Describe the morphology of the red blood cells.
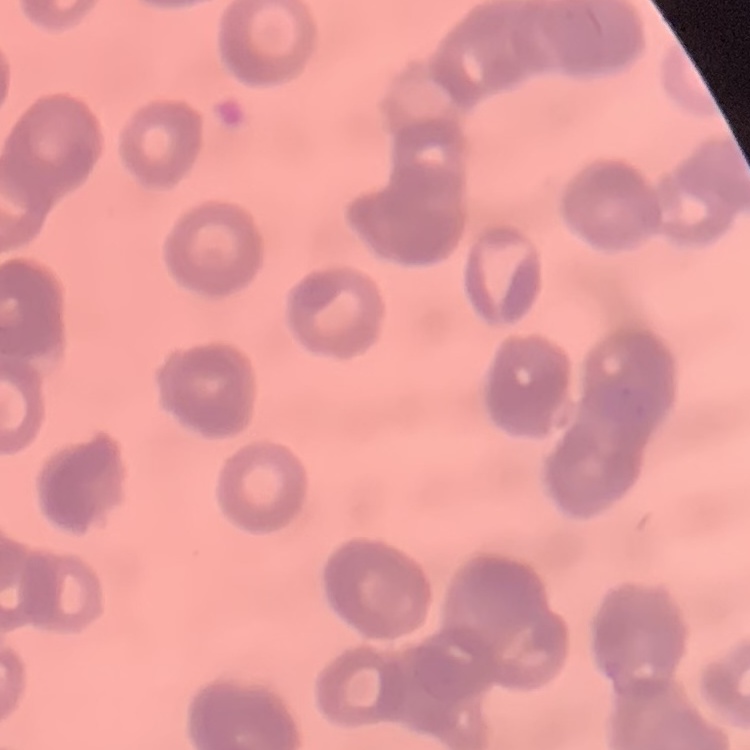

They show rouleaux formation.

stain = Field's or Giemsa
image type = one tile cut from a larger photomicrograph
preparation = thin peripheral smear